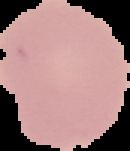

Summary:
  - Image type: segmented cell region with the area outside set to black
  - Malaria status: uninfected
  - Preparation: thin blood film
  - Image size: 130×151 pixels